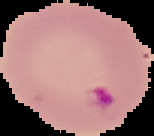

From a thin blood smear. Image is 154×136 pixels. Result: Plasmodium parasites identified. Segmented cell region on a black background.